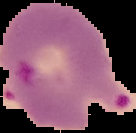

Summary:
  - Image type: segmented cell region with the area outside set to black
  - Image size: 136×133 pixels
  - Malaria status: parasitized
  - Preparation: thin blood smear